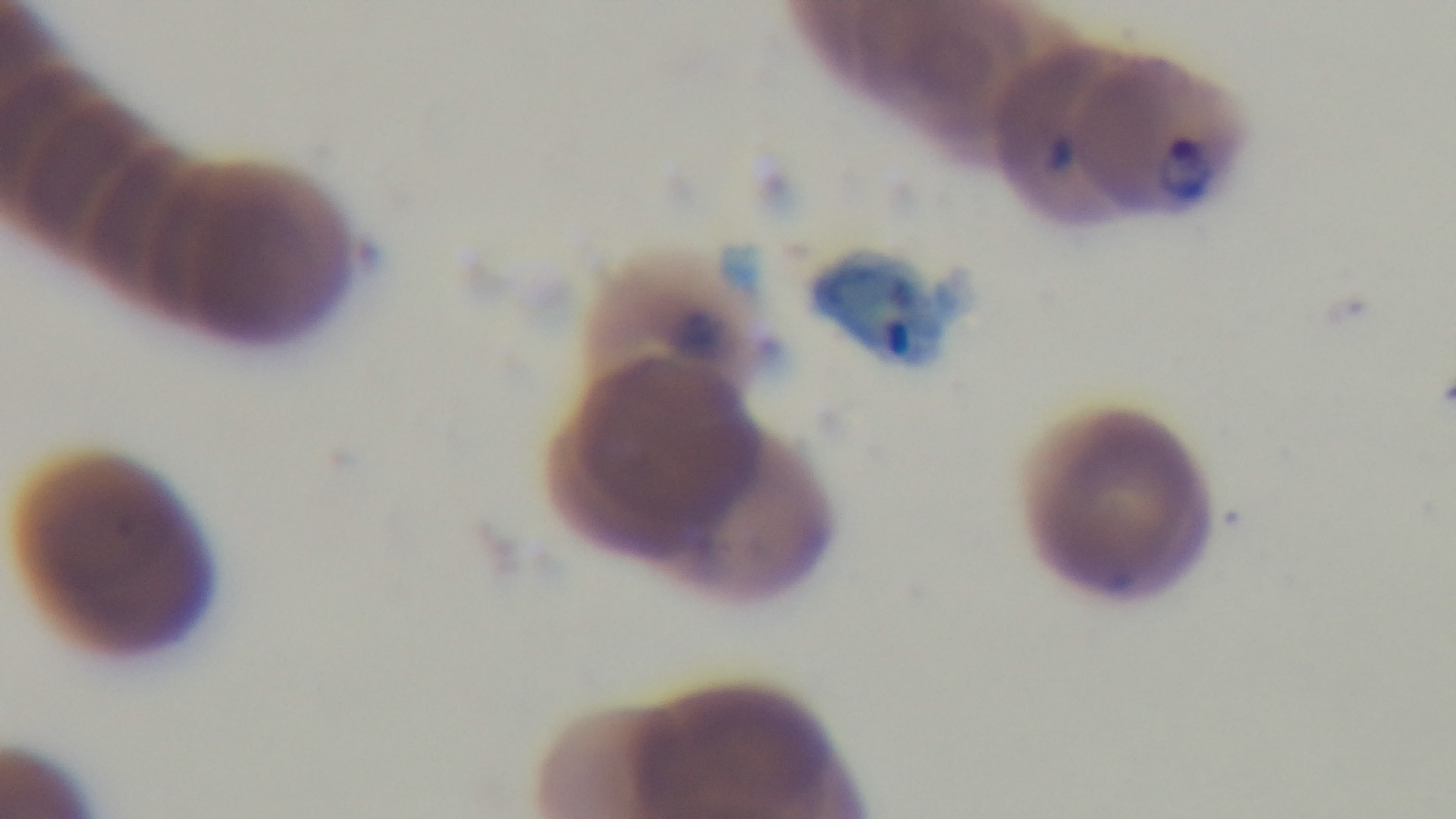
objective = 100x oil immersion
stain = Giemsa
preparation = thin smear
field of view = one from the slide
modality = light microscopy
malaria status = positive
capture = mounted 4K digital camera